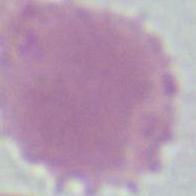

Summary:
  - Magnification: 1000x
  - Identification: erythrocyte
  - Modality: micrograph